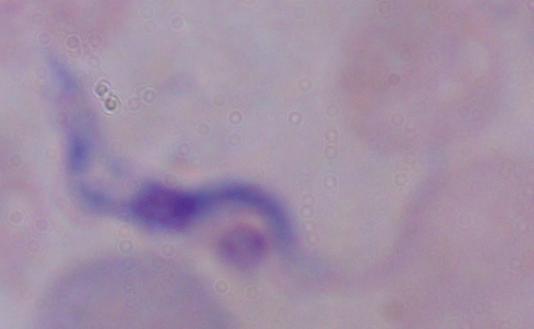

A trypanosome is seen. Photomicrograph. Captured at 1000x magnification.